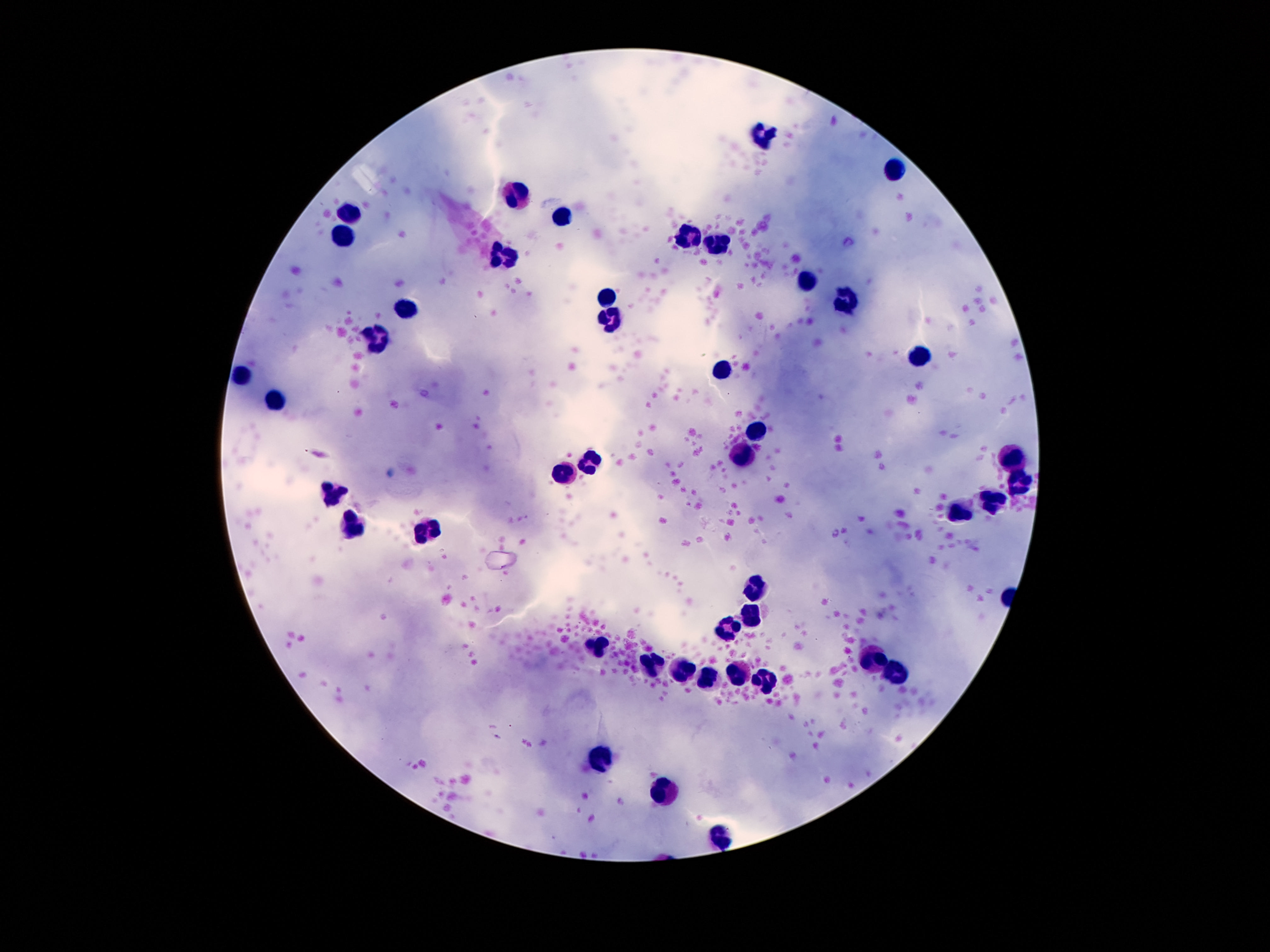
Approximate centers as [x, y] in pixels. Leukocyte locations: [763, 138], [894, 171], [516, 194], [350, 214], [565, 219], [343, 232], [690, 234], [717, 242], [502, 257], [806, 282], [606, 298], [845, 301], [406, 307], [611, 323], [381, 338], [919, 357], [722, 372], [243, 377], [275, 399], [758, 430], [742, 455], [592, 459], [1013, 459], [565, 477], [1019, 482], [332, 491], [992, 504], [960, 514], [354, 527], [427, 529], [756, 588], [752, 617], [729, 627], [597, 649], [876, 663], [650, 669], [684, 672], [736, 674], [706, 676], [895, 677], [765, 679], [600, 754], [665, 792], [722, 833]. Image is 1270×952 pixels. Giemsa stain. 100x magnification. Smartphone photograph taken through the microscope eyepiece. Patient malaria status: negative. One field from this slide. Thick blood film.